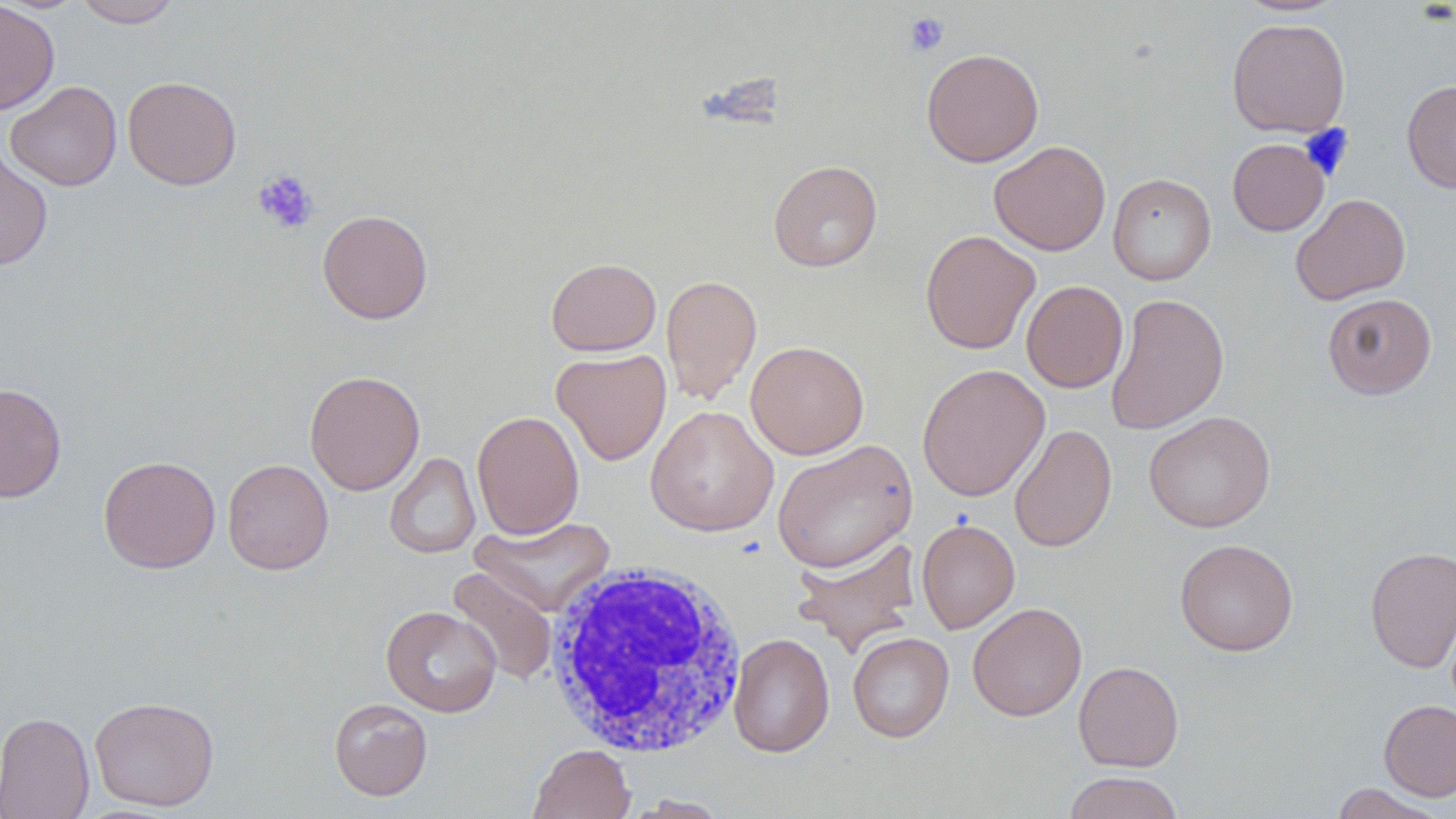
Approximate bounding boxes as (x1, y1, x2, y2) in pixels. White blood cell locations: (543, 559, 749, 758). Uninfected red blood cell locations: (73, 0, 182, 28), (0, 1, 60, 115), (1236, 1, 1346, 16), (1226, 17, 1350, 138), (921, 48, 1044, 167), (122, 75, 242, 190), (1402, 79, 1456, 193), (5, 80, 121, 190), (1227, 138, 1329, 236), (989, 140, 1111, 256), (0, 145, 53, 272), (768, 160, 883, 272), (1108, 173, 1216, 286), (1290, 193, 1411, 305), (317, 209, 433, 324), (920, 230, 1040, 354), (545, 257, 662, 356), (660, 274, 762, 404), (1021, 280, 1128, 393), (1106, 292, 1230, 435), (1322, 293, 1436, 399), (745, 340, 869, 459), (551, 349, 671, 465), (917, 363, 1050, 501), (304, 370, 425, 495), (0, 383, 67, 502), (646, 405, 779, 537), (472, 410, 585, 539), (1144, 410, 1276, 533), (1008, 424, 1117, 552), (771, 439, 918, 573), (385, 452, 480, 559), (97, 455, 221, 573), (222, 459, 333, 574), (470, 516, 615, 617), (916, 518, 1020, 633), (792, 535, 922, 657), (1174, 538, 1298, 656), (1365, 546, 1456, 672), (447, 566, 558, 685), (968, 602, 1087, 722), (381, 605, 502, 717), (847, 631, 954, 742), (728, 633, 834, 757), (1073, 661, 1184, 771), (89, 695, 220, 812), (329, 698, 432, 800), (1379, 699, 1456, 801), (0, 711, 95, 819), (528, 744, 635, 819), (1063, 771, 1185, 819), (1329, 782, 1448, 818), (622, 794, 731, 818). Platelet locations: (904, 12, 949, 56), (252, 169, 319, 234). Slide-level diagnosis: no evidence of blood parasites. One field of a larger specimen. May-Grünwald-Giemsa-stained preparation. Thin blood film. Optical microscopy. Captured at 1000x magnification. Image is 1456×819 pixels.